Classify this cell by malaria status.
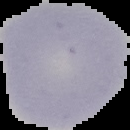

It is uninfected.

image type = segmented cell region with the area outside set to black
preparation = thin blood film
image size = 130×130 pixels